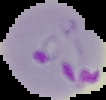

preparation = thin blood smear
image size = 106×100 pixels
image type = segmented cell region on a black background
malaria status = parasitized